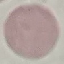 Malaria status: uninfected. Giemsa stain. Cell patch, automatically extracted from a larger field of view and resized to 64 × 64 pixels. Thin smear of blood. Photographed with a smartphone camera at the microscope eyepiece.